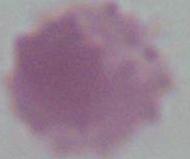

Photomicrograph. An erythrocyte is shown. Captured at 1000x magnification.